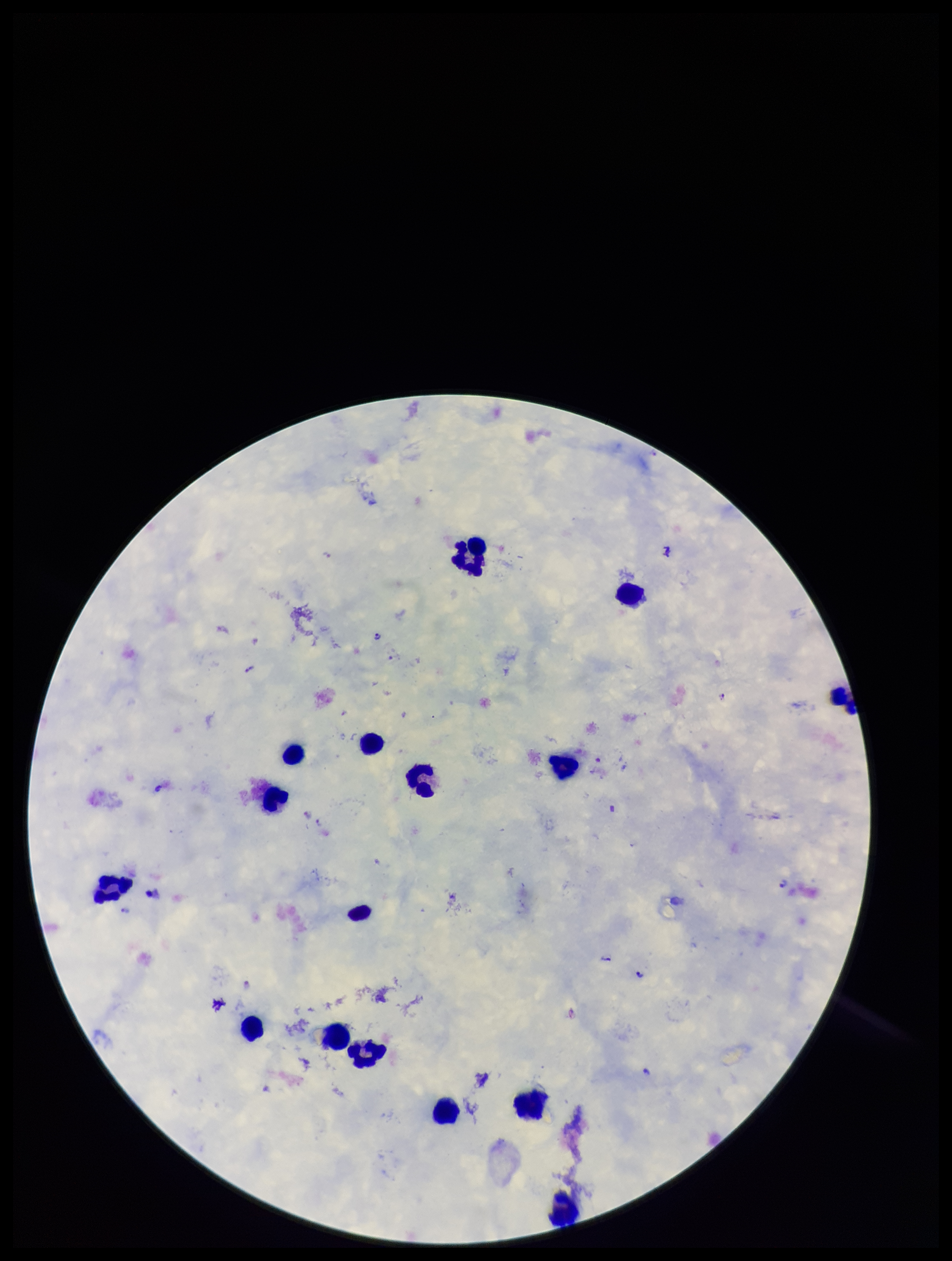
field of view = one from this slide
image size = 952×1261 pixels
parasite count = 15
patient malaria status = positive
species reported for this patient = Plasmodium falciparum
leukocyte count = 16
capture = smartphone photograph through the microscope eyepiece
preparation = thick smear
Plasmodium parasites = seen
stain = Giemsa